Outline each blood parasite and name the species.
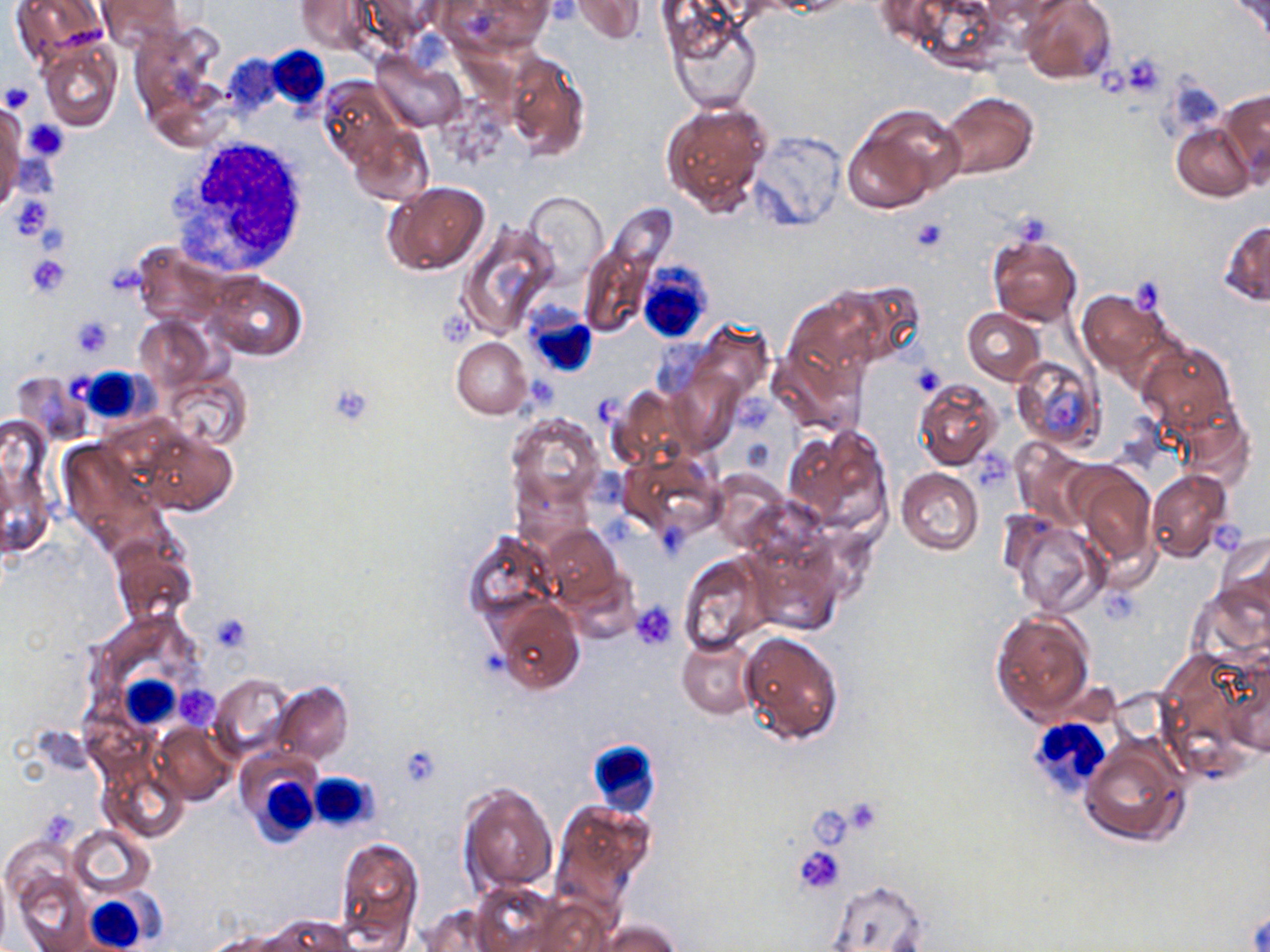

No blood parasites observed.

Summary:
  - Coordinate format: approximate bounding boxes as named x1/y1/x2/y2 corners in pixels
  - Uninfected red blood cell locations: (x1=10, y1=0, x2=108, y2=64), (x1=96, y1=0, x2=186, y2=49), (x1=296, y1=0, x2=372, y2=54), (x1=361, y1=0, x2=448, y2=47), (x1=440, y1=0, x2=552, y2=55), (x1=571, y1=0, x2=646, y2=43), (x1=898, y1=0, x2=1007, y2=69), (x1=1019, y1=0, x2=1116, y2=85), (x1=1228, y1=0, x2=1268, y2=46), (x1=664, y1=7, x2=763, y2=114), (x1=129, y1=23, x2=224, y2=124), (x1=37, y1=37, x2=122, y2=132), (x1=502, y1=51, x2=591, y2=160), (x1=372, y1=53, x2=467, y2=131), (x1=319, y1=77, x2=403, y2=166), (x1=1218, y1=87, x2=1270, y2=183), (x1=939, y1=91, x2=1038, y2=180), (x1=660, y1=99, x2=772, y2=214), (x1=0, y1=101, x2=25, y2=215), (x1=846, y1=105, x2=964, y2=209), (x1=1171, y1=122, x2=1255, y2=201), (x1=348, y1=124, x2=433, y2=206), (x1=748, y1=131, x2=846, y2=232), (x1=383, y1=180, x2=491, y2=275), (x1=523, y1=192, x2=607, y2=279), (x1=457, y1=220, x2=561, y2=339), (x1=1220, y1=221, x2=1270, y2=306), (x1=987, y1=231, x2=1083, y2=328), (x1=580, y1=243, x2=653, y2=336), (x1=133, y1=245, x2=234, y2=329), (x1=205, y1=272, x2=306, y2=360), (x1=845, y1=281, x2=926, y2=364), (x1=787, y1=288, x2=892, y2=382), (x1=1077, y1=290, x2=1175, y2=393), (x1=962, y1=308, x2=1045, y2=384), (x1=134, y1=315, x2=214, y2=390), (x1=689, y1=322, x2=772, y2=405), (x1=451, y1=337, x2=531, y2=419), (x1=1139, y1=342, x2=1235, y2=433), (x1=769, y1=343, x2=864, y2=435), (x1=1011, y1=356, x2=1104, y2=452), (x1=13, y1=370, x2=92, y2=442), (x1=670, y1=371, x2=740, y2=453), (x1=163, y1=372, x2=252, y2=449), (x1=914, y1=379, x2=1001, y2=469), (x1=609, y1=387, x2=700, y2=468), (x1=1170, y1=400, x2=1255, y2=488), (x1=508, y1=411, x2=604, y2=513), (x1=783, y1=423, x2=891, y2=534), (x1=140, y1=428, x2=236, y2=517), (x1=59, y1=441, x2=169, y2=556), (x1=1011, y1=441, x2=1094, y2=527), (x1=617, y1=452, x2=722, y2=540), (x1=1070, y1=463, x2=1156, y2=567), (x1=896, y1=468, x2=982, y2=555), (x1=710, y1=469, x2=791, y2=550), (x1=1145, y1=470, x2=1233, y2=563), (x1=1001, y1=512, x2=1108, y2=618), (x1=540, y1=525, x2=622, y2=611), (x1=462, y1=530, x2=559, y2=624), (x1=1216, y1=531, x2=1270, y2=615), (x1=108, y1=535, x2=199, y2=632), (x1=751, y1=546, x2=844, y2=636), (x1=675, y1=552, x2=774, y2=656), (x1=1188, y1=584, x2=1270, y2=668), (x1=495, y1=602, x2=584, y2=693), (x1=990, y1=609, x2=1096, y2=723), (x1=738, y1=630, x2=843, y2=746), (x1=677, y1=635, x2=760, y2=719), (x1=1218, y1=649, x2=1270, y2=758), (x1=210, y1=674, x2=294, y2=760), (x1=272, y1=682, x2=353, y2=764), (x1=152, y1=722, x2=235, y2=804), (x1=1082, y1=740, x2=1188, y2=847), (x1=100, y1=763, x2=187, y2=843), (x1=459, y1=781, x2=557, y2=895), (x1=552, y1=800, x2=654, y2=910), (x1=68, y1=825, x2=155, y2=899), (x1=332, y1=834, x2=422, y2=951), (x1=13, y1=869, x2=92, y2=950), (x1=827, y1=879, x2=929, y2=951), (x1=470, y1=883, x2=575, y2=952), (x1=417, y1=904, x2=505, y2=951), (x1=262, y1=916, x2=358, y2=952), (x1=593, y1=918, x2=682, y2=952)
  - Platelet locations: (x1=1117, y1=54, x2=1166, y2=95), (x1=1097, y1=65, x2=1138, y2=99), (x1=1, y1=82, x2=35, y2=115), (x1=24, y1=119, x2=69, y2=162), (x1=7, y1=194, x2=53, y2=241), (x1=911, y1=219, x2=948, y2=253), (x1=36, y1=223, x2=69, y2=256), (x1=25, y1=253, x2=70, y2=297), (x1=1131, y1=277, x2=1166, y2=314), (x1=70, y1=315, x2=116, y2=356), (x1=910, y1=362, x2=946, y2=397), (x1=328, y1=382, x2=376, y2=426), (x1=733, y1=397, x2=774, y2=434), (x1=975, y1=446, x2=1007, y2=484), (x1=1213, y1=521, x2=1245, y2=551), (x1=1101, y1=587, x2=1144, y2=624), (x1=631, y1=602, x2=678, y2=650), (x1=208, y1=613, x2=252, y2=653), (x1=178, y1=685, x2=219, y2=726), (x1=399, y1=745, x2=444, y2=789), (x1=849, y1=802, x2=877, y2=832), (x1=813, y1=808, x2=847, y2=846), (x1=793, y1=845, x2=845, y2=894)
  - White blood cell locations: (x1=266, y1=41, x2=334, y2=106), (x1=168, y1=133, x2=314, y2=278), (x1=638, y1=263, x2=712, y2=344), (x1=523, y1=302, x2=598, y2=380), (x1=77, y1=368, x2=151, y2=422), (x1=120, y1=675, x2=180, y2=729), (x1=1028, y1=723, x2=1112, y2=801), (x1=585, y1=738, x2=659, y2=817), (x1=236, y1=752, x2=325, y2=847), (x1=310, y1=773, x2=376, y2=829), (x1=84, y1=893, x2=148, y2=949)
  - Slide-level diagnosis: negative for blood parasites
  - Image size: 1270×952 pixels
  - Modality: optical microscopy
  - Magnification: 1000x
  - Field of view: single
  - Preparation: thin blood film
  - Stain: May-Grünwald-Giemsa